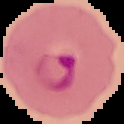

Summary:
  - Preparation: thin blood smear
  - Image size: 124×124 pixels
  - Image type: segmented cell region with the area outside set to black
  - Malaria status: parasitized